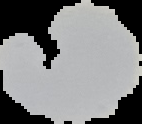

Malaria status: uninfected. Image is 142×124 pixels. From a thin blood film. Cell region segmented out of the field of view; the surrounding area is masked to black.